Report the malaria status of this cell.
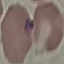

It is parasitized.

Cell patch, automatically extracted from a larger field of view and resized to 64 × 64 pixels. Thin blood film. Giemsa-stained preparation. Acquired by smartphone through the microscope eyepiece.